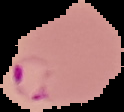

{
  "image_size": "124×112 pixels",
  "image_type": "cell region segmented out of the field of view; surrounding area masked to black",
  "preparation": "thin blood film",
  "malaria_status": "parasitized"
}